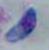 Photomicrograph. 1000x magnification. Toxoplasma gondii is seen.